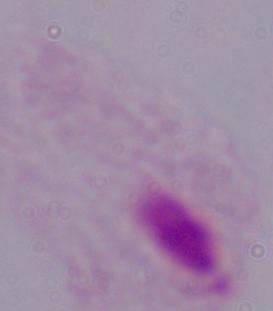

Summary:
  - Magnification: 1000x
  - Modality: micrograph
  - Identification: trichomonad